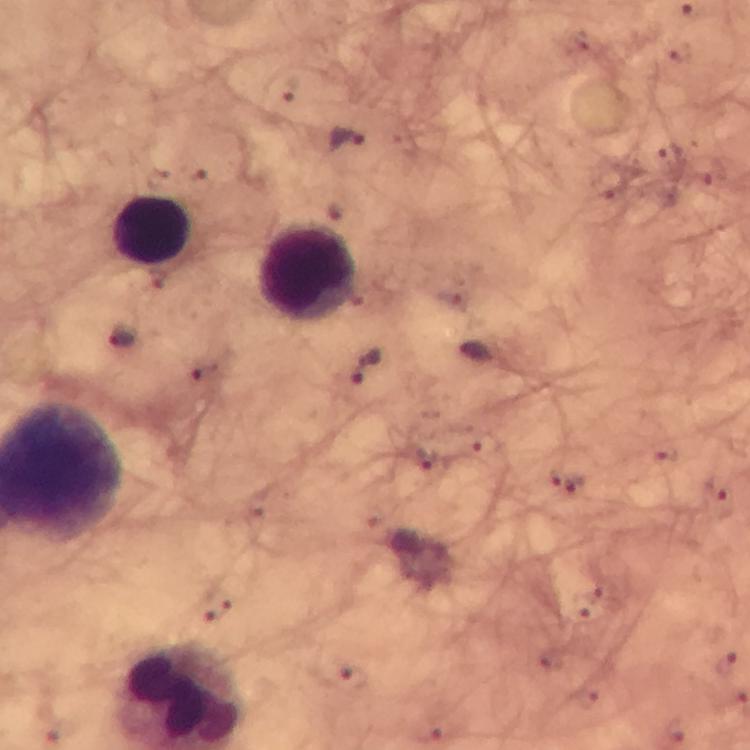
Approximate centers as (x, y) in pixels. Leukocyte locations: (152, 229), (308, 272). Plasmodium parasite locations: (681, 54), (345, 138), (123, 335), (366, 368), (427, 460), (567, 480), (728, 665), (351, 676), (434, 731). Smartphone photograph taken through a microscope. Cropped region of a single field of view. Image is 750×750 pixels. From a malaria diagnostic workup. Immersion oil was used. Thick smear. Giemsa stain. 100x magnification.